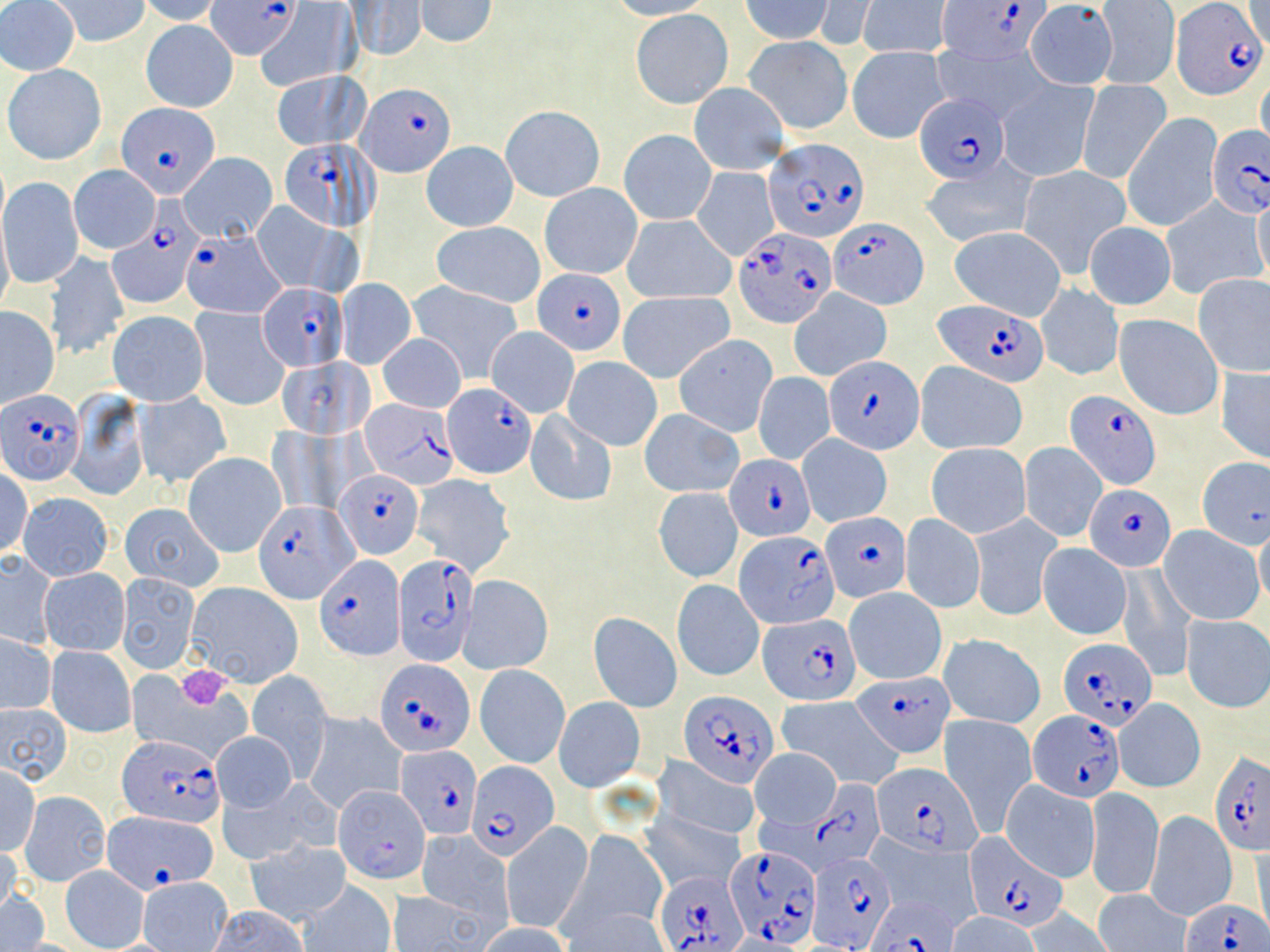 Approximate bounding boxes as (x1, y1, x2, y2) in pixels. Plasmodium falciparum-infected red blood cell locations (subset): (206, 1, 297, 61), (935, 1, 1051, 66), (1170, 2, 1265, 99), (358, 83, 456, 178), (916, 93, 1009, 183), (118, 103, 218, 198), (1207, 126, 1270, 219), (763, 137, 871, 242), (280, 139, 375, 232), (109, 218, 203, 309), (832, 218, 928, 307), (735, 228, 835, 329), (180, 229, 281, 317), (534, 267, 626, 355), (257, 283, 347, 371), (933, 299, 1050, 387), (825, 355, 924, 455), (443, 383, 537, 480), (1065, 388, 1163, 491), (0, 390, 85, 485), (361, 398, 456, 489), (726, 453, 815, 541), (335, 469, 424, 557), (1085, 485, 1176, 572), (254, 501, 354, 601), (821, 512, 911, 602), (735, 531, 841, 629), (392, 554, 479, 667), (318, 555, 404, 657), (759, 614, 860, 703), (1056, 637, 1156, 730), (375, 659, 473, 756), (853, 673, 954, 758), (679, 690, 779, 786), (1027, 709, 1125, 802), (117, 735, 223, 827), (397, 744, 482, 839), (1209, 753, 1270, 858), (467, 761, 557, 859), (873, 762, 981, 856), (809, 779, 886, 868), (103, 810, 219, 893), (962, 835, 1068, 931), (728, 845, 819, 948), (804, 846, 895, 951), (656, 869, 746, 952), (868, 893, 959, 952), (1180, 898, 1270, 952). Platelet locations: (173, 665, 233, 710). Uninfected red blood cell locations (subset): (50, 0, 149, 48), (136, 0, 224, 26), (604, 0, 716, 21), (0, 1, 80, 75), (347, 1, 425, 61), (414, 1, 498, 48), (737, 1, 832, 43), (814, 1, 875, 48), (859, 1, 948, 59), (1093, 2, 1179, 89), (1243, 2, 1268, 49), (1024, 3, 1115, 88), (257, 5, 359, 90), (632, 10, 732, 107), (140, 19, 239, 114), (744, 36, 852, 134), (933, 44, 1056, 125), (847, 46, 950, 143), (5, 65, 103, 165), (270, 69, 370, 152), (1256, 72, 1270, 157), (997, 80, 1098, 182), (1078, 80, 1170, 183), (690, 82, 789, 174), (501, 105, 604, 201), (1122, 114, 1221, 230), (620, 130, 716, 225), (421, 142, 518, 231), (179, 152, 277, 242), (922, 160, 1036, 247), (1017, 164, 1132, 279), (69, 165, 160, 254), (692, 168, 778, 260), (1, 178, 82, 289), (540, 183, 642, 279), (1252, 193, 1270, 289), (1159, 197, 1265, 300), (252, 202, 341, 293), (621, 214, 736, 304), (0, 216, 13, 316), (292, 216, 365, 300), (433, 221, 545, 309), (1083, 221, 1176, 310), (949, 226, 1068, 320), (45, 251, 129, 361), (1193, 273, 1270, 377), (336, 277, 417, 370), (409, 281, 525, 383), (1036, 285, 1124, 382), (791, 289, 891, 380), (618, 292, 733, 382), (0, 307, 60, 408), (191, 307, 291, 412), (107, 309, 207, 404), (1114, 315, 1222, 422), (485, 326, 578, 418), (376, 332, 467, 413), (673, 335, 778, 437), (563, 356, 662, 450), (277, 357, 374, 440), (914, 362, 1029, 455), (1215, 365, 1270, 465), (753, 371, 835, 464), (67, 390, 150, 501), (134, 391, 232, 489), (639, 409, 745, 497), (526, 410, 617, 507), (267, 426, 351, 516), (797, 433, 892, 526), (1019, 442, 1107, 543), (926, 443, 1030, 539), (184, 452, 286, 556), (1196, 456, 1269, 545), (1, 468, 32, 559), (411, 475, 516, 576), (653, 487, 745, 584), (18, 493, 113, 580), (120, 503, 224, 592), (899, 513, 985, 613), (968, 514, 1061, 621), (1253, 518, 1270, 616), (1160, 524, 1263, 625), (1038, 544, 1130, 639), (0, 551, 58, 647), (39, 567, 129, 656), (1116, 567, 1195, 680), (117, 573, 200, 674), (459, 576, 554, 675), (672, 579, 765, 681), (185, 582, 303, 689), (845, 588, 946, 683), (587, 613, 682, 712), (1181, 616, 1270, 713), (1, 633, 57, 714), (940, 633, 1043, 729), (46, 647, 135, 737), (476, 665, 569, 768), (126, 667, 256, 766), (246, 671, 333, 778), (554, 697, 645, 792), (775, 697, 900, 788), (1114, 700, 1205, 793), (0, 703, 71, 786), (303, 712, 406, 814), (940, 715, 1037, 834), (212, 731, 297, 811), (751, 749, 841, 829), (654, 756, 761, 844), (1, 766, 40, 854), (999, 779, 1099, 882), (216, 783, 323, 864), (1026, 785, 1147, 893), (1085, 786, 1163, 901), (19, 791, 110, 886), (1144, 811, 1238, 921), (641, 812, 745, 894), (501, 821, 592, 935), (570, 830, 667, 933), (416, 831, 512, 924), (866, 835, 983, 928), (247, 839, 351, 924), (0, 841, 22, 918), (1248, 845, 1270, 937), (61, 866, 148, 950), (138, 876, 233, 952), (299, 879, 396, 951), (1093, 889, 1191, 952), (1, 890, 49, 951), (388, 891, 489, 951), (562, 905, 672, 952), (207, 906, 310, 952), (1021, 907, 1116, 951), (947, 913, 1041, 952), (476, 923, 571, 952). Slide-level diagnosis: Plasmodium falciparum. Optical microscopy. 1000x magnification. Image is 1270×952 pixels. Thin blood smear. May-Grünwald-Giemsa stain. One field of a larger specimen.